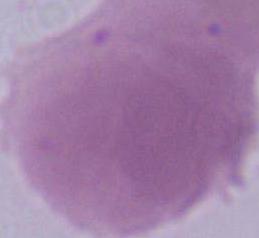
identification = red blood cell
modality = photomicrograph
magnification = 1000x